Assess for malaria.
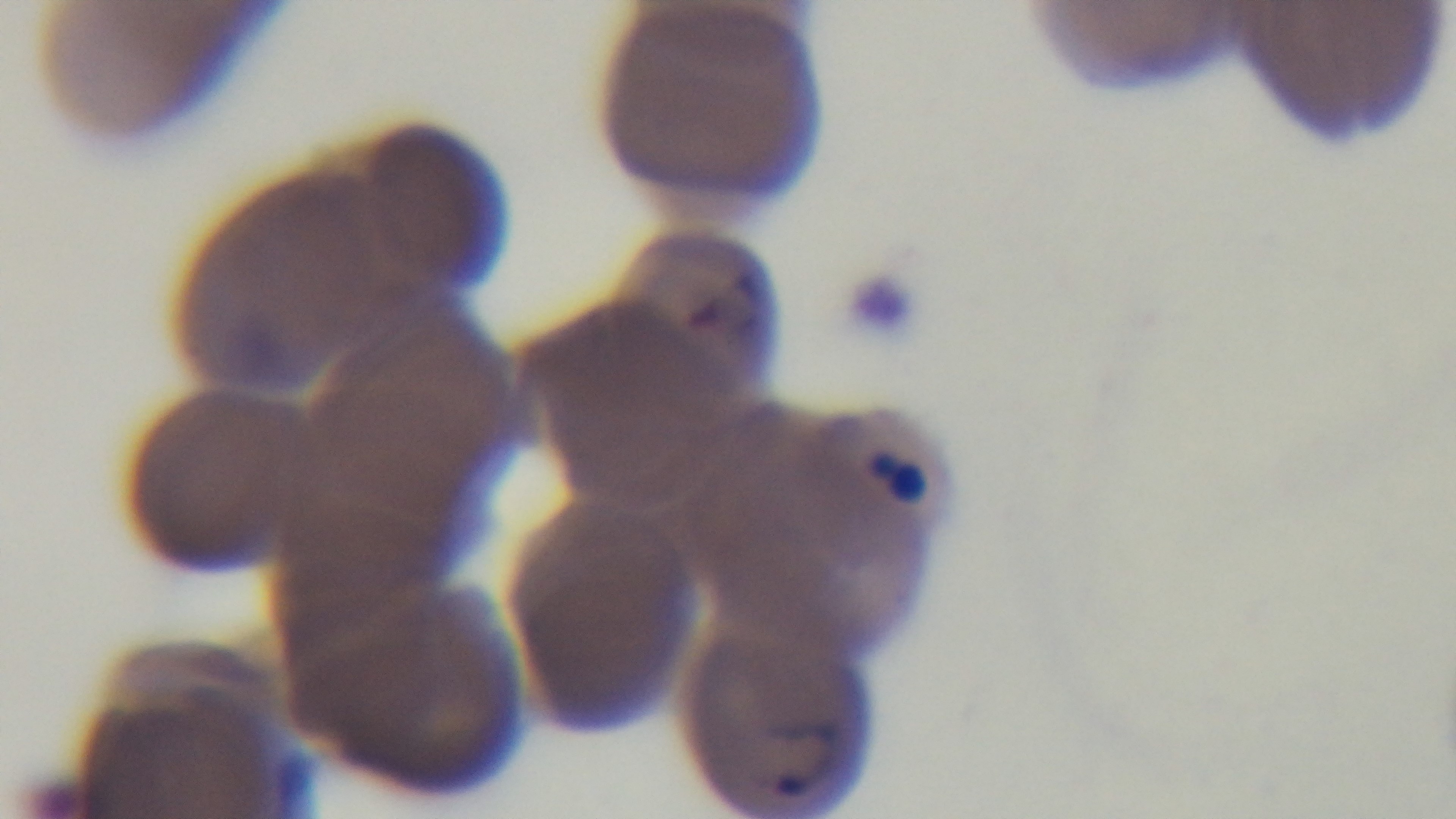
Infected.

Summary:
  - Field of view: one from the slide
  - Modality: light microscopy
  - Objective: 100x oil immersion
  - Capture: mounted 4K digital camera
  - Stain: Giemsa
  - Preparation: thin